Locate and identify every blood parasite.
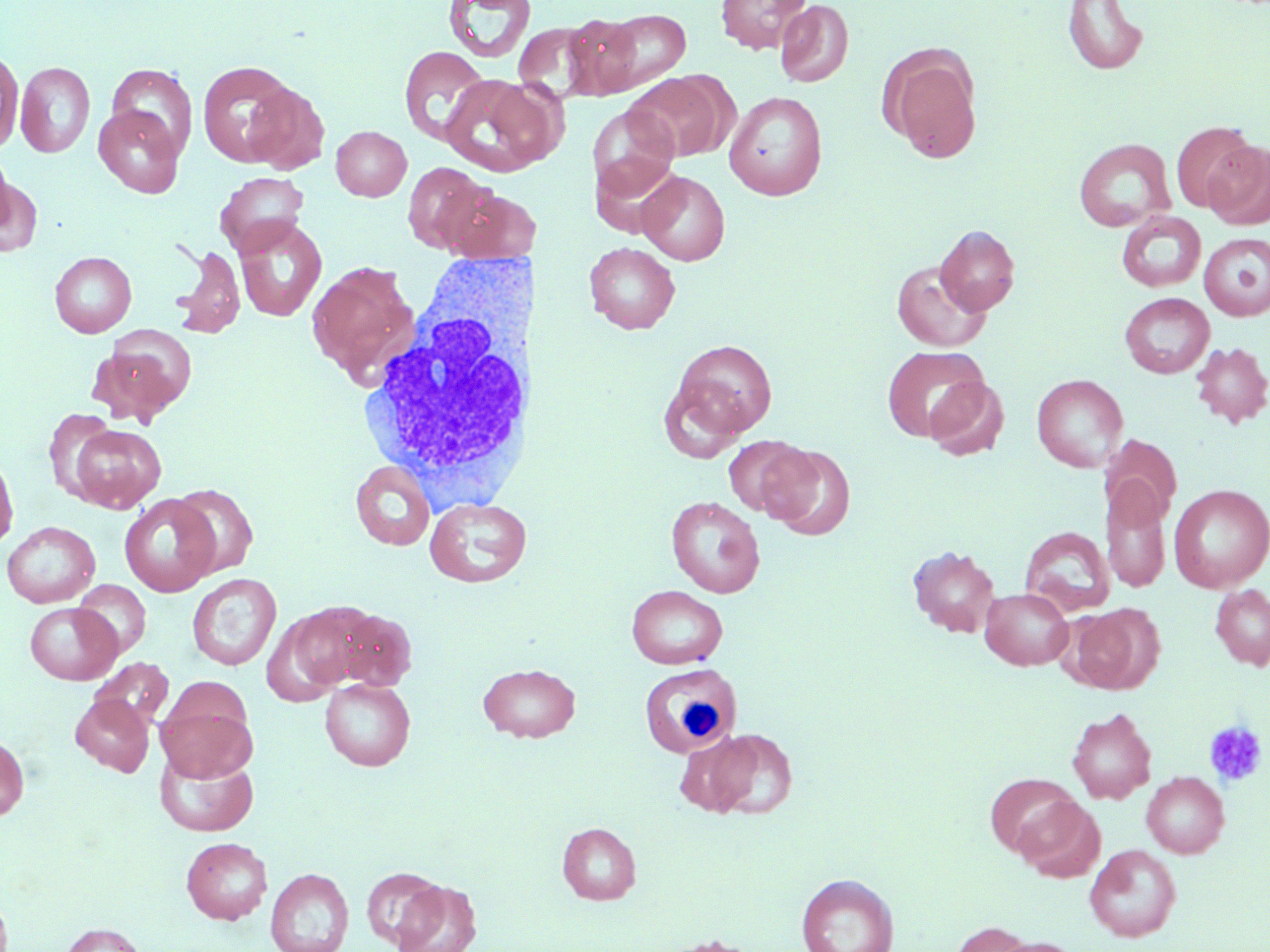
No blood parasites seen.

Approximate bounding boxes as named x1/y1/x2/y2 corners in pixels. Platelet locations: (x1=1203, y1=720, x2=1268, y2=788). Uninfected red blood cell locations: (x1=716, y1=0, x2=811, y2=53), (x1=775, y1=0, x2=853, y2=88), (x1=444, y1=1, x2=535, y2=63), (x1=1063, y1=1, x2=1149, y2=75), (x1=597, y1=9, x2=690, y2=92), (x1=561, y1=13, x2=646, y2=99), (x1=513, y1=22, x2=599, y2=102), (x1=880, y1=44, x2=983, y2=164), (x1=399, y1=46, x2=489, y2=145), (x1=0, y1=49, x2=23, y2=153), (x1=197, y1=60, x2=299, y2=166), (x1=16, y1=62, x2=95, y2=158), (x1=107, y1=63, x2=198, y2=159), (x1=626, y1=73, x2=728, y2=162), (x1=440, y1=75, x2=559, y2=177), (x1=243, y1=81, x2=329, y2=175), (x1=724, y1=91, x2=828, y2=200), (x1=587, y1=104, x2=679, y2=202), (x1=93, y1=105, x2=184, y2=197), (x1=1170, y1=121, x2=1258, y2=213), (x1=331, y1=125, x2=411, y2=201), (x1=1073, y1=138, x2=1176, y2=232), (x1=1203, y1=140, x2=1270, y2=230), (x1=1, y1=147, x2=17, y2=243), (x1=592, y1=152, x2=682, y2=235), (x1=402, y1=161, x2=495, y2=254), (x1=638, y1=170, x2=730, y2=265), (x1=0, y1=171, x2=41, y2=258), (x1=215, y1=172, x2=309, y2=257), (x1=446, y1=186, x2=533, y2=265), (x1=1117, y1=211, x2=1206, y2=292), (x1=234, y1=218, x2=327, y2=322), (x1=935, y1=225, x2=1020, y2=315), (x1=1198, y1=232, x2=1270, y2=321), (x1=584, y1=242, x2=680, y2=334), (x1=170, y1=245, x2=246, y2=338), (x1=50, y1=251, x2=136, y2=337), (x1=892, y1=260, x2=991, y2=352), (x1=307, y1=262, x2=419, y2=384), (x1=1120, y1=292, x2=1214, y2=378), (x1=98, y1=326, x2=197, y2=420), (x1=672, y1=339, x2=777, y2=438), (x1=1190, y1=341, x2=1270, y2=429), (x1=882, y1=345, x2=989, y2=442), (x1=1032, y1=373, x2=1128, y2=472), (x1=924, y1=376, x2=1010, y2=461), (x1=657, y1=379, x2=747, y2=462), (x1=43, y1=408, x2=119, y2=500), (x1=69, y1=425, x2=165, y2=512), (x1=1100, y1=434, x2=1181, y2=528), (x1=722, y1=436, x2=813, y2=518), (x1=761, y1=444, x2=856, y2=541), (x1=0, y1=448, x2=18, y2=554), (x1=351, y1=461, x2=435, y2=550), (x1=1101, y1=480, x2=1171, y2=593), (x1=170, y1=484, x2=258, y2=578), (x1=1168, y1=484, x2=1270, y2=592), (x1=119, y1=494, x2=220, y2=596), (x1=666, y1=496, x2=765, y2=598), (x1=424, y1=497, x2=531, y2=588), (x1=2, y1=521, x2=100, y2=608), (x1=1020, y1=526, x2=1115, y2=617), (x1=907, y1=545, x2=1001, y2=637), (x1=187, y1=573, x2=281, y2=670), (x1=73, y1=580, x2=151, y2=658), (x1=1210, y1=584, x2=1270, y2=670), (x1=626, y1=585, x2=728, y2=669), (x1=980, y1=587, x2=1074, y2=670), (x1=25, y1=602, x2=122, y2=684), (x1=1069, y1=604, x2=1163, y2=694), (x1=270, y1=605, x2=363, y2=700), (x1=327, y1=608, x2=418, y2=691), (x1=90, y1=657, x2=174, y2=731), (x1=477, y1=662, x2=580, y2=742), (x1=320, y1=678, x2=416, y2=770), (x1=155, y1=689, x2=257, y2=783), (x1=70, y1=694, x2=154, y2=776), (x1=1067, y1=707, x2=1157, y2=804), (x1=702, y1=728, x2=798, y2=820), (x1=0, y1=733, x2=29, y2=822), (x1=155, y1=748, x2=259, y2=836), (x1=1141, y1=771, x2=1229, y2=858), (x1=985, y1=773, x2=1079, y2=858), (x1=1015, y1=796, x2=1105, y2=882), (x1=557, y1=822, x2=641, y2=905), (x1=181, y1=837, x2=272, y2=924), (x1=1085, y1=844, x2=1181, y2=942), (x1=362, y1=866, x2=447, y2=949), (x1=265, y1=868, x2=354, y2=952), (x1=796, y1=873, x2=898, y2=952), (x1=392, y1=880, x2=482, y2=952), (x1=948, y1=920, x2=1034, y2=952), (x1=59, y1=923, x2=146, y2=952), (x1=658, y1=934, x2=762, y2=952), (x1=990, y1=937, x2=1084, y2=952). White blood cell locations: (x1=358, y1=243, x2=560, y2=491), (x1=638, y1=664, x2=741, y2=758). Slide-level diagnosis: no evidence of blood parasites. May-Grünwald-Giemsa stain. Image is 1270×952 pixels. Thin blood smear. Light microscopy. Captured at 1000x magnification. Single field of view.